Report the malaria status of this cell.
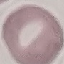

Uninfected.

capture: smartphone through the microscope eyepiece
image_type: cell patch, automatically extracted from a larger field of view and resized to 64 × 64 pixels
preparation: thin smear
stain: Giemsa